Assess this cell for malaria.
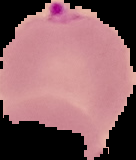
It is parasitized.

Summary:
  - Image size: 136×160 pixels
  - Image type: segmented cell region on a black background
  - Preparation: thin blood smear